Name the parasite shown.
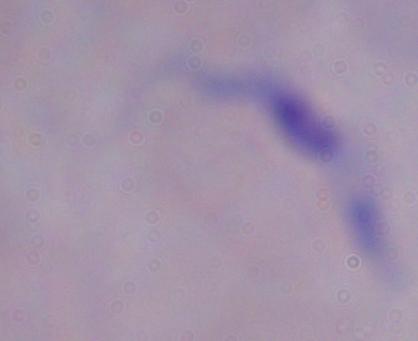
A trypanosome.

Summary:
  - Magnification: 1000x
  - Modality: photomicrograph